State which parasite is depicted.
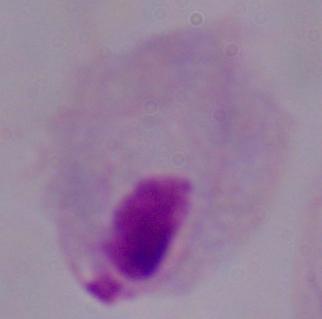
A trichomonad.

1000x magnification. Micrograph.